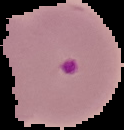
Summary:
  - Image type: segmented cell region on a black background
  - Result: Plasmodium parasites detected
  - Image size: 124×130 pixels
  - Preparation: thin blood smear